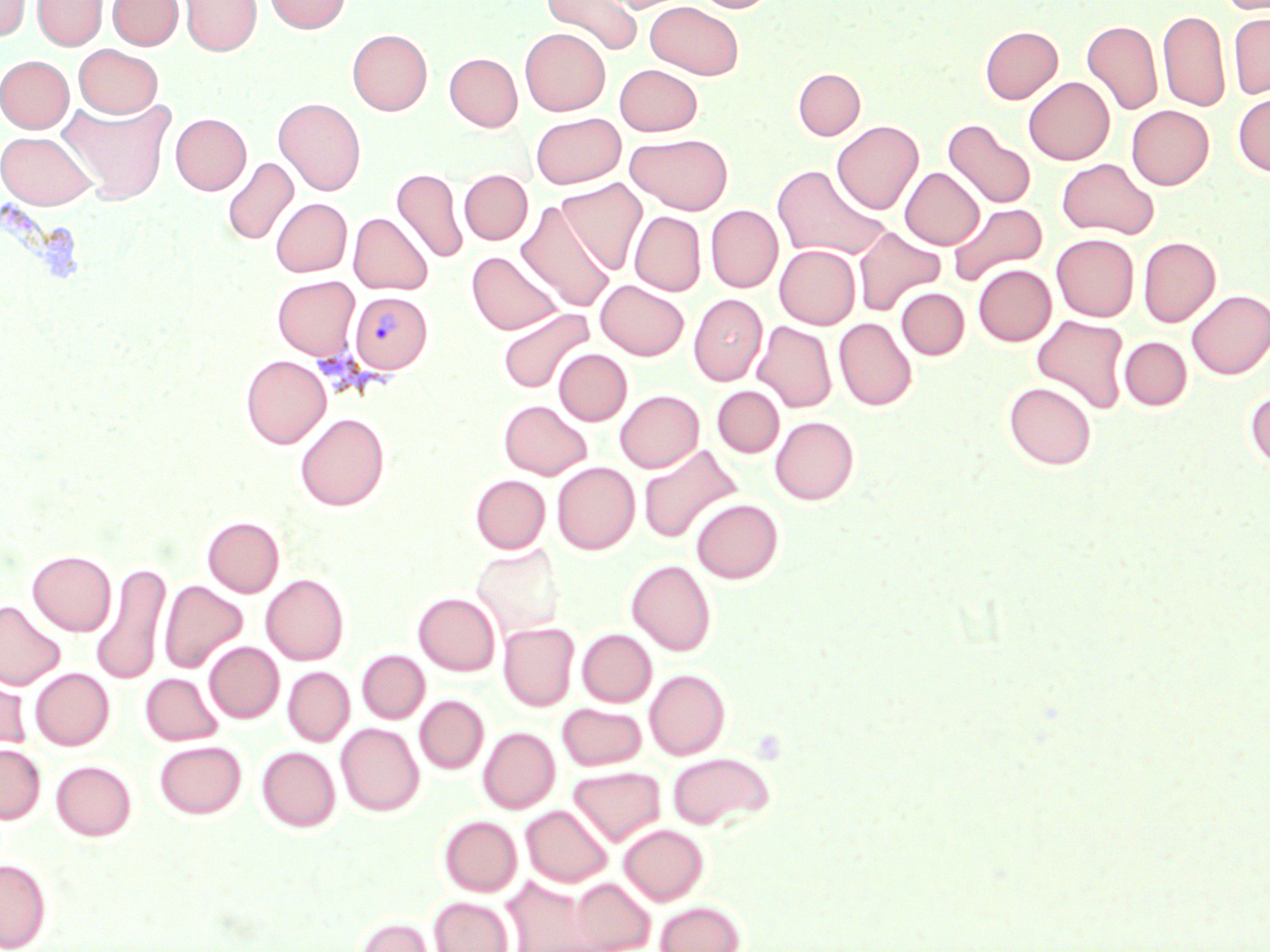

Approximate bounding boxes as (x1,y1)-(x2,y2) corner pairs in pixels. Plasmodium vivax-infected red blood cell locations: (350,292)-(433,373). Uninfected red blood cell locations: (33,0)-(107,50), (108,0)-(183,50), (179,0)-(261,56), (265,0)-(351,33), (541,0)-(643,56), (600,0)-(689,13), (691,0)-(775,13), (1217,0)-(1270,14), (1,1)-(31,41), (645,1)-(744,79), (1158,10)-(1230,112), (1228,12)-(1270,99), (1082,20)-(1162,115), (980,26)-(1062,103), (520,28)-(610,116), (347,29)-(432,115), (74,44)-(162,118), (445,53)-(522,131), (0,55)-(73,132), (614,64)-(702,136), (793,68)-(865,139), (1024,77)-(1114,165), (1233,92)-(1270,176), (60,97)-(176,205), (273,97)-(366,195), (1127,105)-(1213,189), (531,112)-(625,189), (170,113)-(251,195), (943,120)-(1036,209), (832,121)-(923,214), (0,131)-(96,209), (625,133)-(733,214), (222,157)-(298,246), (1057,158)-(1159,239), (772,164)-(890,261), (901,167)-(984,249), (391,168)-(468,263), (459,170)-(532,244), (558,177)-(648,275), (271,198)-(352,277), (516,200)-(615,313), (948,203)-(1047,286), (705,205)-(783,292), (630,211)-(706,295), (348,213)-(433,295), (853,226)-(946,316), (1052,233)-(1139,321), (1138,237)-(1220,326), (775,245)-(860,329), (467,251)-(563,334), (973,264)-(1056,345), (272,275)-(360,359), (596,280)-(689,360), (897,288)-(969,359), (1186,290)-(1270,379), (689,294)-(767,386), (497,308)-(594,393), (1032,315)-(1130,413), (834,318)-(917,410), (754,321)-(836,412), (1120,337)-(1192,410), (554,349)-(631,425), (241,355)-(330,448), (1004,382)-(1097,469), (712,386)-(784,457), (616,390)-(703,472), (1245,390)-(1270,471), (499,400)-(591,479), (295,413)-(389,510), (770,416)-(859,504), (638,445)-(742,544), (552,462)-(639,554), (470,474)-(550,553), (691,499)-(783,583), (203,517)-(284,597), (471,544)-(566,639), (27,550)-(116,636), (627,559)-(716,656), (92,561)-(171,685), (261,574)-(349,665), (160,580)-(247,673), (414,592)-(500,675), (0,600)-(65,691), (499,623)-(579,711), (577,629)-(656,707), (204,642)-(284,723), (357,650)-(429,723), (283,667)-(354,746), (30,668)-(114,750), (0,669)-(31,754), (645,669)-(730,760), (140,673)-(223,746), (415,696)-(489,774), (557,703)-(647,770), (336,723)-(424,816), (478,727)-(560,813), (154,741)-(246,818), (0,744)-(45,823), (257,747)-(340,832), (667,752)-(774,830), (51,761)-(136,840), (569,766)-(666,846), (521,804)-(612,887), (439,815)-(522,896), (620,824)-(708,905), (0,859)-(51,951), (503,876)-(595,952), (569,878)-(655,952), (430,897)-(513,952), (655,901)-(744,952), (354,916)-(436,952). Slide-level diagnosis: Plasmodium vivax. Thin blood smear. Image is 1270×952 pixels. Light microscopy. May-Grünwald-Giemsa stain. 1000x magnification. One field of a larger specimen.